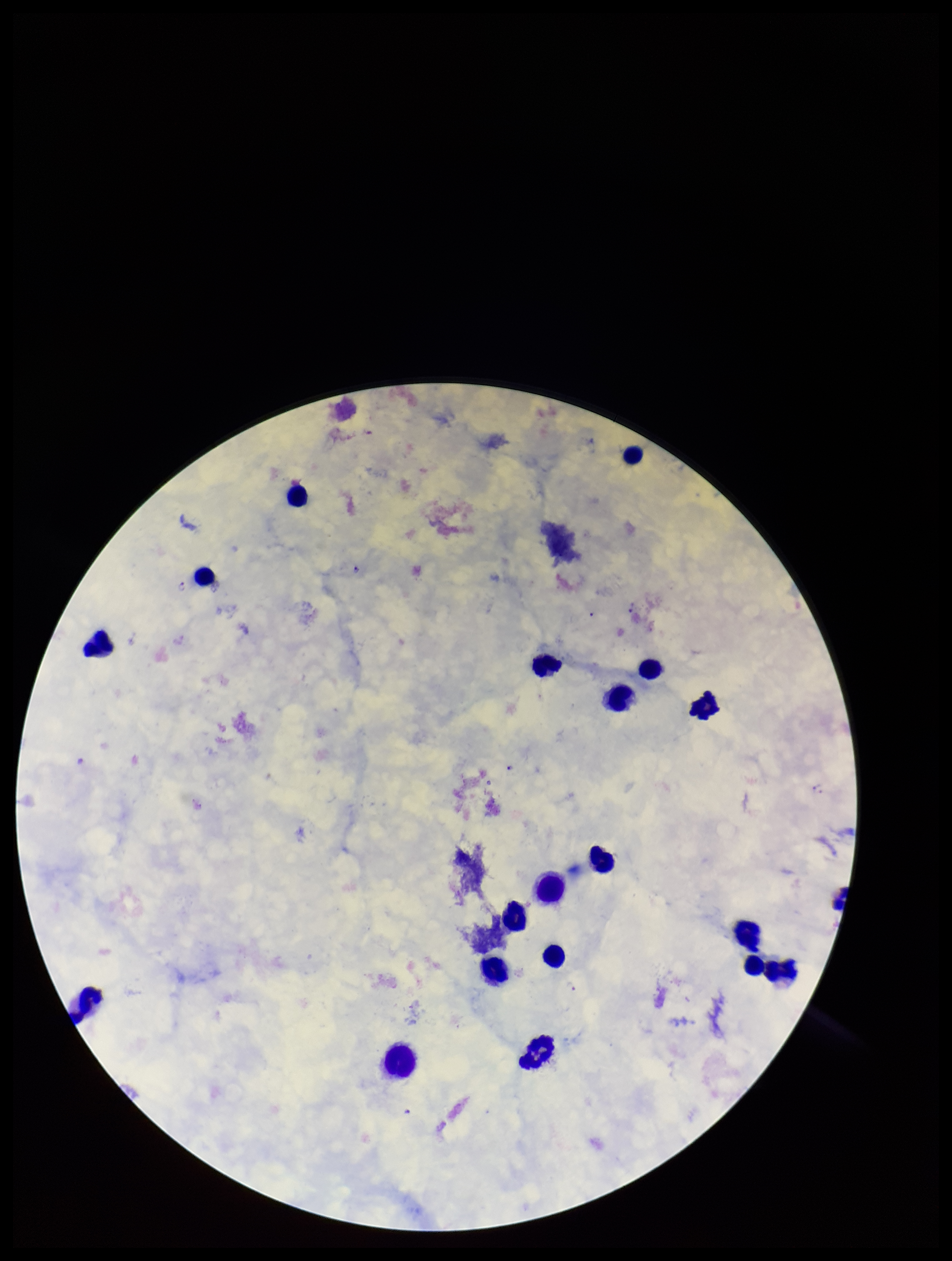
species_reported_for_this_patient: Plasmodium falciparum
patient_malaria_status: positive
leukocyte_count: 17
image_size: 952×1261 pixels
stain: Giemsa
field_of_view: one from this slide
capture: smartphone photograph through the microscope eyepiece
preparation: thick blood smear
parasite_count: 3
plasmodium_parasites: identified